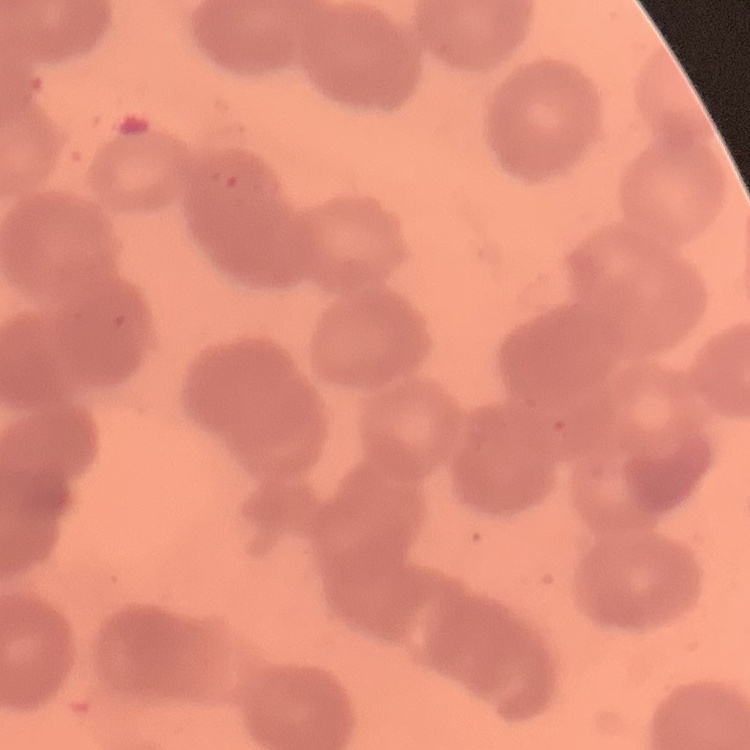
Summary:
  - Erythrocyte morphology: rouleaux formation
  - Image type: one tile cut from a larger photomicrograph
  - Stain: Field's or Giemsa
  - Preparation: thin blood film